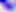 Micrograph. Toxoplasma gondii is shown. Captured at 400x magnification.